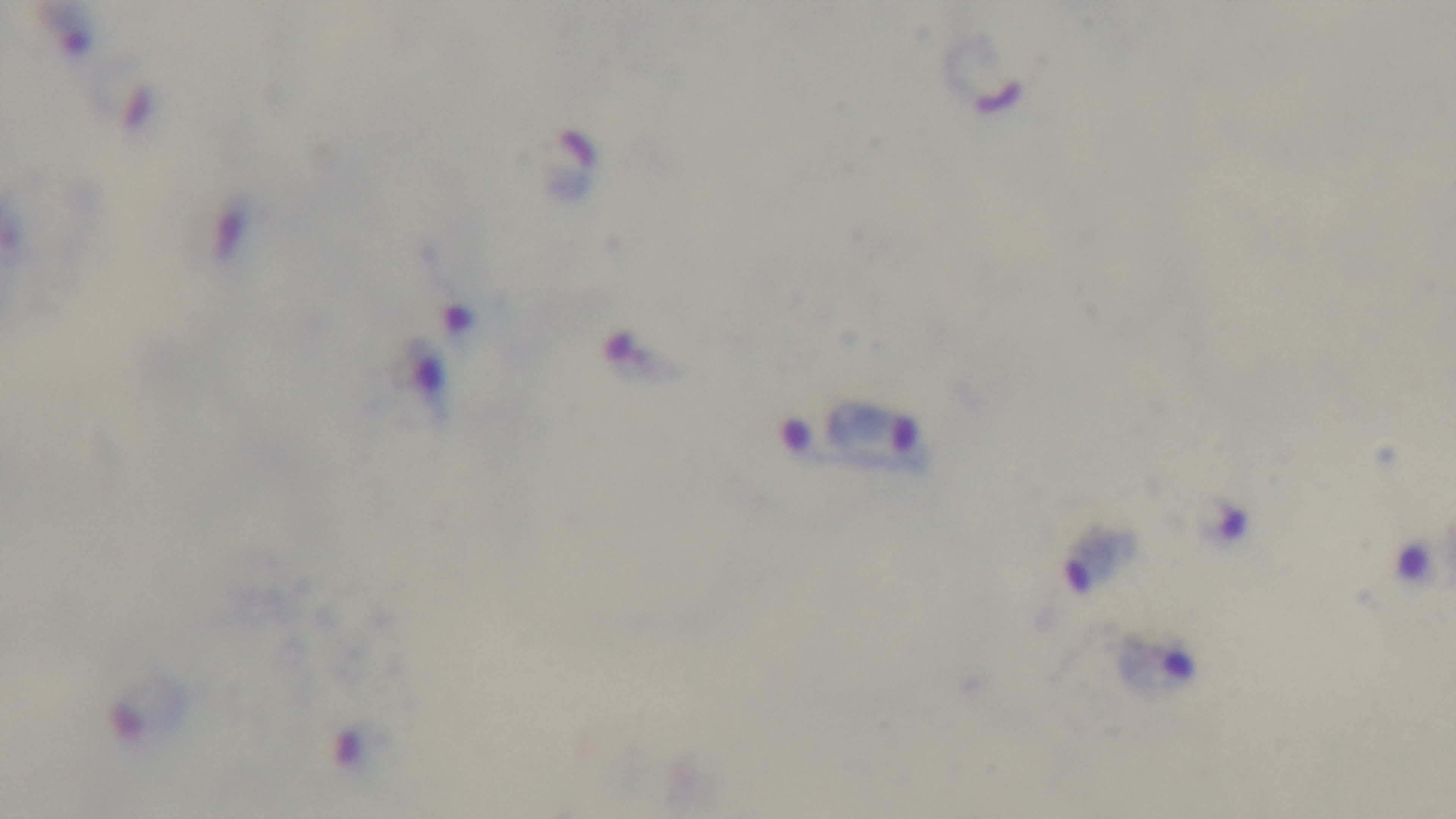
Malaria status: infected. Preparation: thick. One field from the slide. 100x oil-immersion objective. Light microscopy. Giemsa stain. Captured with a mounted 4K digital camera.